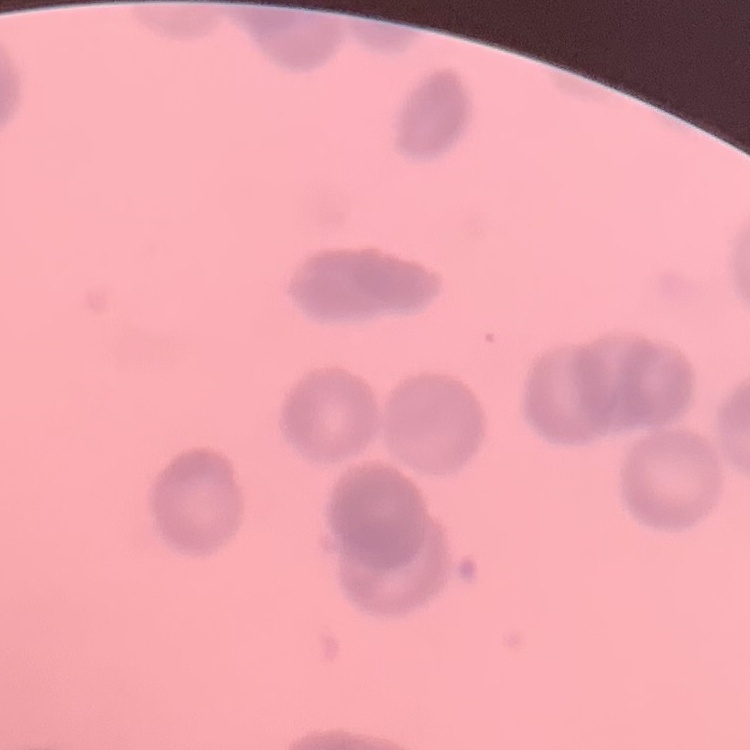
Summary:
  - Erythrocyte morphology: rouleaux formation
  - Image type: one tile cut from a larger photomicrograph
  - Preparation: thin blood film
  - Stain: Field's or Giemsa